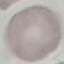

Summary:
  - Result: no malaria parasites seen
  - Image type: cell patch, automatically extracted from a larger field of view and resized to 64 × 64 pixels
  - Capture: smartphone camera at the microscope eyepiece
  - Preparation: thin blood smear
  - Stain: Giemsa